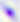

modality: micrograph
magnification: 400x
identification: Toxoplasma gondii